Name the parasite shown.
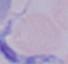
A trypanosome.

modality = photomicrograph
magnification = 1000x